Locate every Plasmodium falciparum-infected red blood cell.
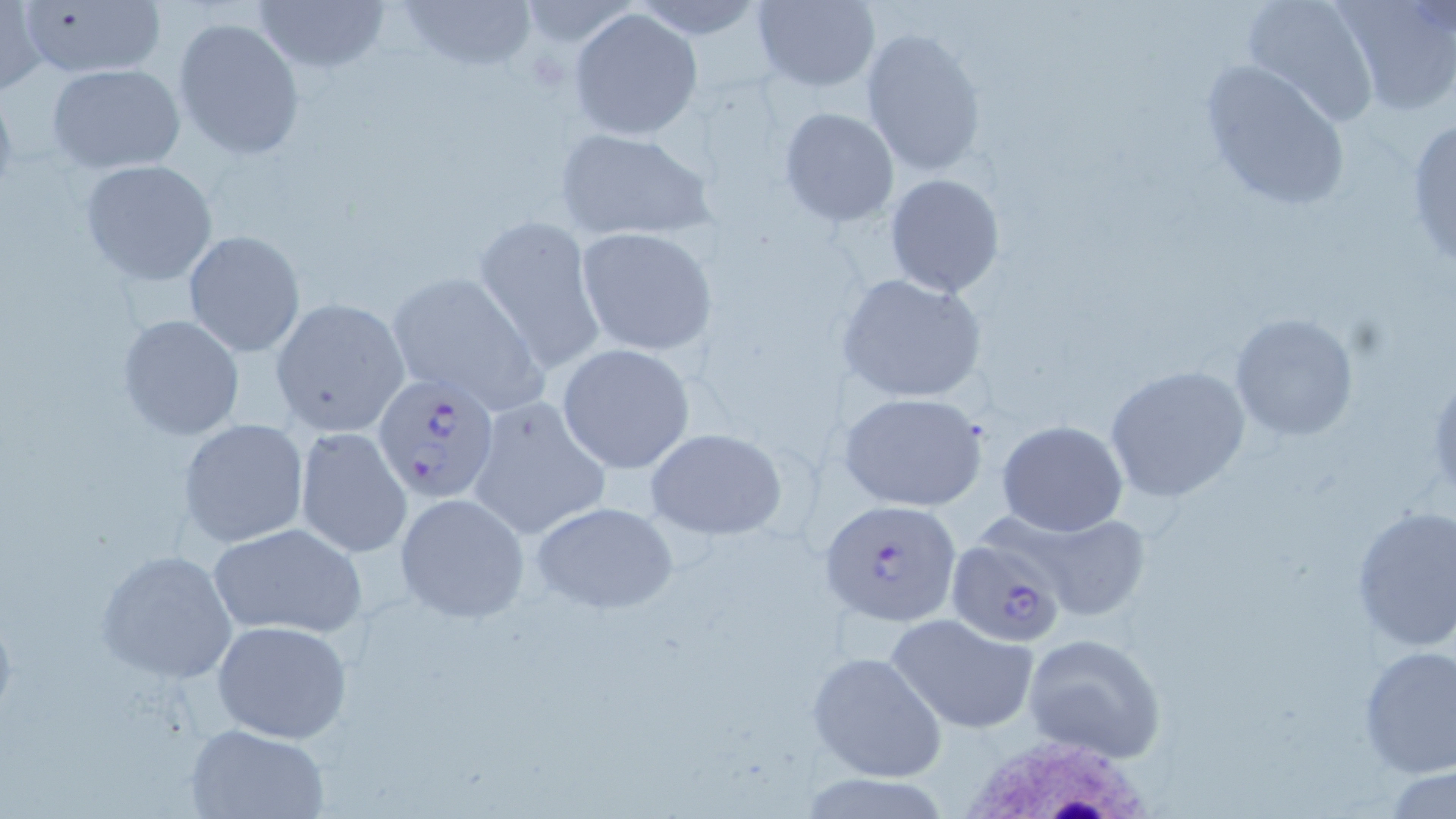

Approximate bounding boxes as named x1/y1/x2/y2 corners in pixels.
Plasmodium falciparum-infected red blood cells: (x1=373, y1=371, x2=502, y2=506), (x1=820, y1=498, x2=960, y2=626), (x1=945, y1=535, x2=1070, y2=647).

Uninfected red blood cell locations: (x1=12, y1=0, x2=167, y2=80), (x1=250, y1=0, x2=390, y2=76), (x1=392, y1=0, x2=536, y2=76), (x1=753, y1=0, x2=880, y2=91), (x1=1238, y1=0, x2=1383, y2=126), (x1=0, y1=1, x2=49, y2=97), (x1=1333, y1=2, x2=1456, y2=118), (x1=569, y1=7, x2=705, y2=141), (x1=173, y1=16, x2=306, y2=161), (x1=861, y1=28, x2=987, y2=178), (x1=1199, y1=58, x2=1352, y2=213), (x1=47, y1=63, x2=188, y2=173), (x1=778, y1=107, x2=899, y2=227), (x1=1404, y1=116, x2=1456, y2=273), (x1=552, y1=126, x2=717, y2=241), (x1=79, y1=159, x2=219, y2=286), (x1=883, y1=173, x2=1006, y2=299), (x1=473, y1=213, x2=606, y2=376), (x1=575, y1=227, x2=717, y2=356), (x1=182, y1=230, x2=306, y2=358), (x1=383, y1=271, x2=548, y2=413), (x1=836, y1=274, x2=987, y2=405), (x1=268, y1=298, x2=410, y2=437), (x1=1230, y1=312, x2=1359, y2=441), (x1=117, y1=313, x2=246, y2=442), (x1=556, y1=342, x2=695, y2=473), (x1=1104, y1=364, x2=1251, y2=501), (x1=840, y1=390, x2=988, y2=512), (x1=466, y1=394, x2=610, y2=542), (x1=178, y1=418, x2=309, y2=547), (x1=996, y1=420, x2=1129, y2=537), (x1=645, y1=427, x2=786, y2=540), (x1=295, y1=428, x2=412, y2=558), (x1=394, y1=492, x2=530, y2=623), (x1=530, y1=501, x2=679, y2=613), (x1=1350, y1=504, x2=1456, y2=651), (x1=1013, y1=507, x2=1153, y2=617), (x1=206, y1=521, x2=367, y2=639), (x1=95, y1=548, x2=240, y2=683), (x1=886, y1=612, x2=1040, y2=732), (x1=212, y1=620, x2=351, y2=744), (x1=1022, y1=631, x2=1168, y2=763), (x1=1357, y1=645, x2=1456, y2=777), (x1=808, y1=650, x2=947, y2=784), (x1=183, y1=722, x2=330, y2=818). White blood cell locations: (x1=949, y1=727, x2=1169, y2=818). Slide-level diagnosis: Plasmodium falciparum. Image is 1456×819 pixels. Thin blood smear. One field of a larger specimen. 1000x magnification. Light microscopy. May-Grünwald-Giemsa stain.